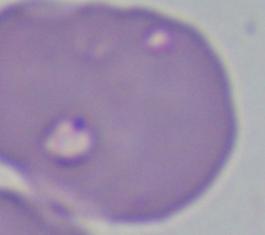
magnification = 1000x
identification = Babesia
modality = photomicrograph